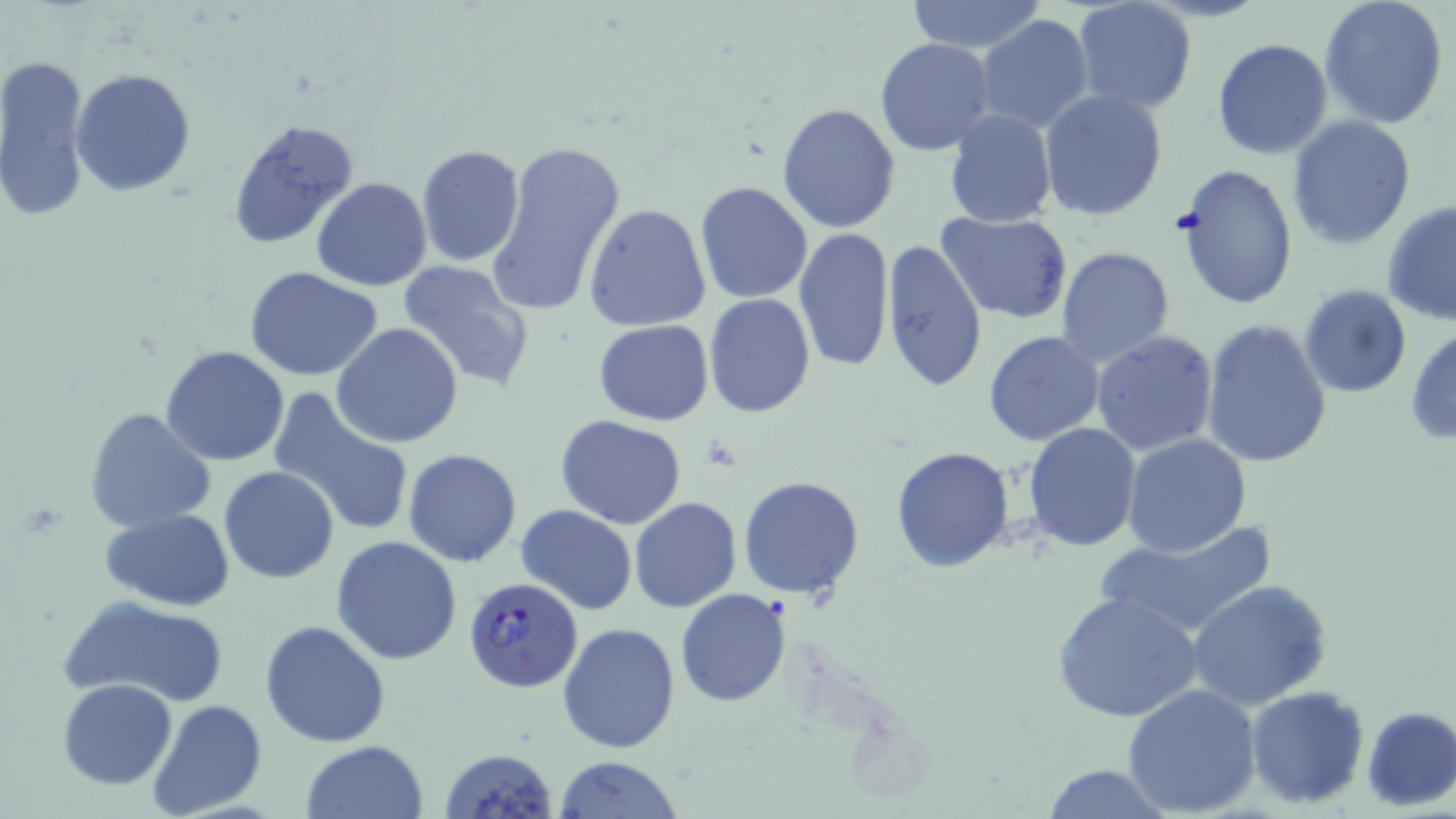 Approximate bounding boxes as named x1/y1/x2/y2 corners in pixels. Plasmodium falciparum-infected red blood cell locations: (x1=464, y1=578, x2=582, y2=693). Uninfected red blood cell locations: (x1=903, y1=0, x2=1047, y2=53), (x1=1071, y1=0, x2=1199, y2=116), (x1=1318, y1=0, x2=1451, y2=129), (x1=975, y1=14, x2=1093, y2=134), (x1=874, y1=38, x2=996, y2=155), (x1=1212, y1=38, x2=1333, y2=159), (x1=0, y1=52, x2=91, y2=223), (x1=70, y1=69, x2=196, y2=195), (x1=1038, y1=88, x2=1169, y2=223), (x1=776, y1=101, x2=903, y2=234), (x1=944, y1=109, x2=1058, y2=227), (x1=1287, y1=115, x2=1417, y2=250), (x1=226, y1=117, x2=359, y2=252), (x1=483, y1=139, x2=626, y2=317), (x1=415, y1=144, x2=524, y2=267), (x1=1173, y1=163, x2=1299, y2=311), (x1=311, y1=176, x2=433, y2=292), (x1=695, y1=181, x2=813, y2=303), (x1=1381, y1=200, x2=1456, y2=327), (x1=584, y1=203, x2=711, y2=332), (x1=936, y1=211, x2=1073, y2=322), (x1=794, y1=228, x2=895, y2=374), (x1=881, y1=239, x2=988, y2=394), (x1=1055, y1=246, x2=1176, y2=369), (x1=397, y1=260, x2=536, y2=392), (x1=244, y1=267, x2=386, y2=381), (x1=1298, y1=285, x2=1413, y2=399), (x1=703, y1=294, x2=815, y2=418), (x1=1201, y1=319, x2=1333, y2=468), (x1=590, y1=320, x2=714, y2=424), (x1=331, y1=324, x2=462, y2=449), (x1=1406, y1=326, x2=1455, y2=446), (x1=983, y1=331, x2=1104, y2=445), (x1=1090, y1=331, x2=1219, y2=458), (x1=161, y1=345, x2=290, y2=465), (x1=267, y1=387, x2=415, y2=539), (x1=84, y1=407, x2=216, y2=534), (x1=556, y1=415, x2=687, y2=529), (x1=1024, y1=423, x2=1143, y2=552), (x1=1123, y1=434, x2=1252, y2=556), (x1=891, y1=446, x2=1017, y2=572), (x1=402, y1=448, x2=521, y2=567), (x1=218, y1=465, x2=340, y2=583), (x1=738, y1=475, x2=865, y2=600), (x1=629, y1=498, x2=742, y2=614), (x1=515, y1=505, x2=637, y2=615), (x1=100, y1=509, x2=235, y2=610), (x1=1092, y1=519, x2=1282, y2=639), (x1=331, y1=536, x2=461, y2=666), (x1=1186, y1=579, x2=1333, y2=710), (x1=675, y1=589, x2=791, y2=708), (x1=1053, y1=592, x2=1206, y2=726), (x1=64, y1=595, x2=232, y2=708), (x1=259, y1=621, x2=390, y2=748), (x1=557, y1=622, x2=681, y2=755), (x1=57, y1=678, x2=178, y2=788), (x1=1122, y1=683, x2=1261, y2=816), (x1=1244, y1=685, x2=1369, y2=809), (x1=147, y1=699, x2=267, y2=819), (x1=1360, y1=706, x2=1456, y2=811), (x1=301, y1=740, x2=429, y2=819), (x1=439, y1=747, x2=557, y2=819), (x1=554, y1=756, x2=684, y2=818), (x1=1039, y1=763, x2=1172, y2=819). Slide-level diagnosis: Plasmodium falciparum. Optical microscopy. Thin blood smear. May-Grünwald-Giemsa-stained preparation. One field of a larger specimen. Image is 1456×819 pixels. 1000x magnification.